Give the extent of all Plasmodium vivax-infected red blood cells.
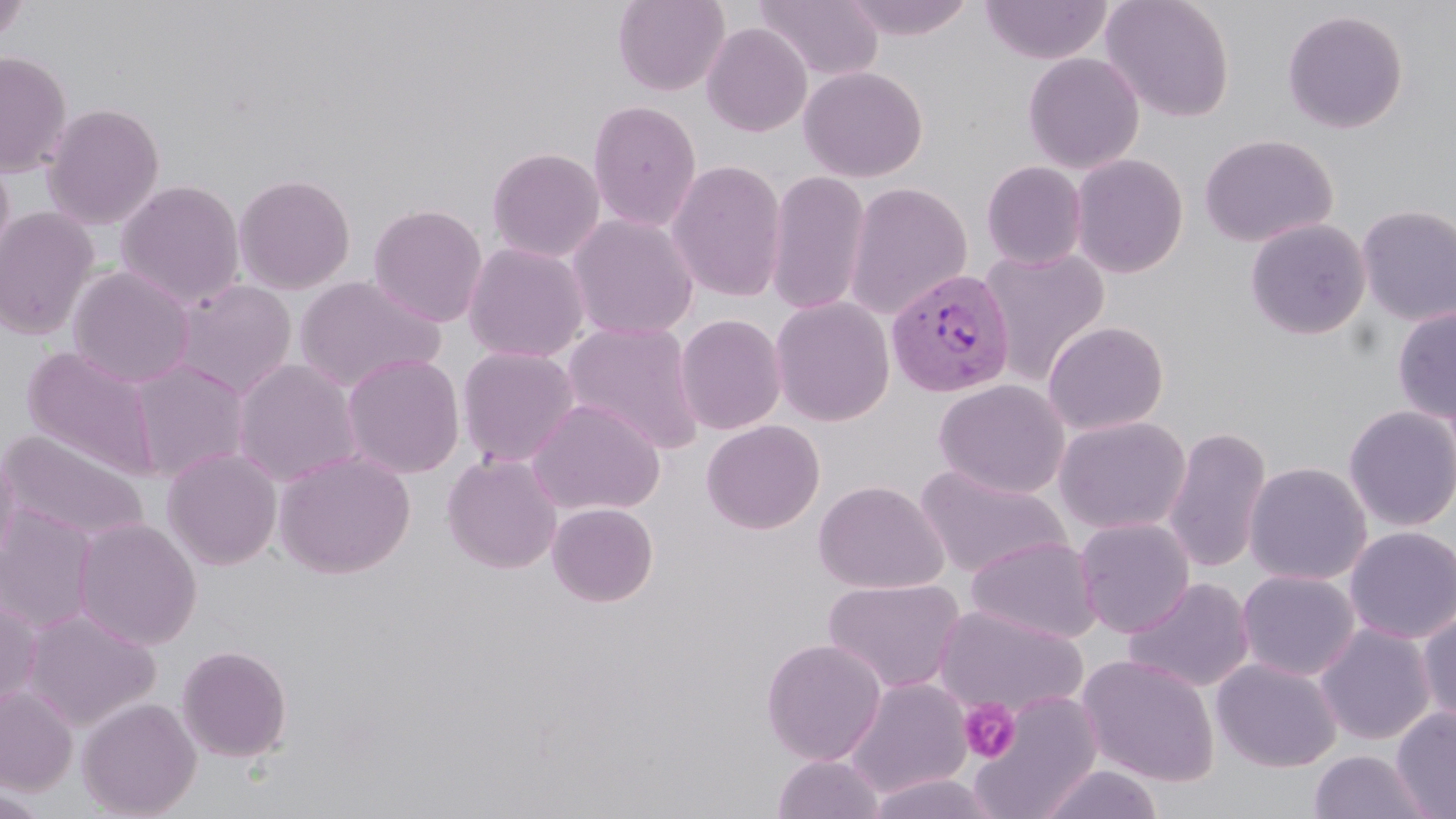

Approximate bounding boxes as (x1,y1)-(x2,y2) corner pairs in pixels.
Plasmodium vivax-infected red blood cells: (886,267)-(1016,398).

Summary:
  - Uninfected red blood cell locations: (612,0)-(729,97), (752,0)-(883,82), (838,0)-(978,40), (1101,0)-(1235,122), (0,1)-(32,47), (980,1)-(1112,65), (1282,9)-(1408,134), (701,22)-(813,137), (0,51)-(72,177), (1022,52)-(1145,173), (799,65)-(928,182), (587,100)-(702,232), (43,102)-(165,230), (1199,133)-(1338,248), (487,147)-(605,263), (0,153)-(15,280), (1070,153)-(1189,278), (667,159)-(788,303), (982,161)-(1088,269), (765,170)-(871,316), (233,173)-(356,294), (116,179)-(245,308), (844,181)-(973,320), (367,204)-(488,327), (1356,204)-(1456,326), (0,207)-(100,340), (565,213)-(699,340), (1245,218)-(1371,339), (463,241)-(590,363), (979,246)-(1110,385), (67,265)-(196,388), (292,275)-(445,392), (169,278)-(298,399), (770,296)-(895,426), (1392,307)-(1456,425), (675,314)-(787,435), (1042,320)-(1169,435), (562,321)-(704,455), (694,321)-(813,523), (22,345)-(160,479), (456,346)-(580,467), (341,353)-(465,479), (129,359)-(250,483), (232,359)-(362,487), (933,379)-(1070,499), (528,398)-(665,516), (1342,405)-(1456,532), (1054,416)-(1191,535), (701,419)-(825,535), (1162,425)-(1272,575), (0,430)-(149,543), (162,447)-(283,571), (0,448)-(21,569), (274,449)-(415,579), (441,452)-(562,574), (1243,461)-(1372,585), (914,465)-(1072,580), (814,479)-(949,594), (547,502)-(658,607), (0,504)-(98,634), (73,517)-(202,650), (1073,517)-(1195,638), (1344,526)-(1456,644), (965,535)-(1101,644), (1236,569)-(1360,681), (1124,576)-(1255,693), (822,578)-(967,695), (0,596)-(42,713), (932,604)-(1088,719), (22,607)-(160,731), (1417,608)-(1456,729), (1315,624)-(1435,745), (760,639)-(886,765), (176,644)-(292,762), (1077,654)-(1220,786), (1211,657)-(1342,773), (845,677)-(972,798), (0,687)-(78,794), (968,690)-(1103,818), (77,697)-(202,818), (1391,705)-(1456,818), (1308,750)-(1435,819), (772,753)-(884,818), (1035,764)-(1165,819), (864,772)-(999,819)
  - Platelet locations: (959,698)-(1020,763)
  - Slide-level diagnosis: Plasmodium vivax
  - Field of view: single
  - Magnification: 1000x
  - Preparation: thin blood smear
  - Image size: 1456×819 pixels
  - Modality: light microscopy
  - Stain: May-Grünwald-Giemsa